Describe the morphology of the red blood cells.
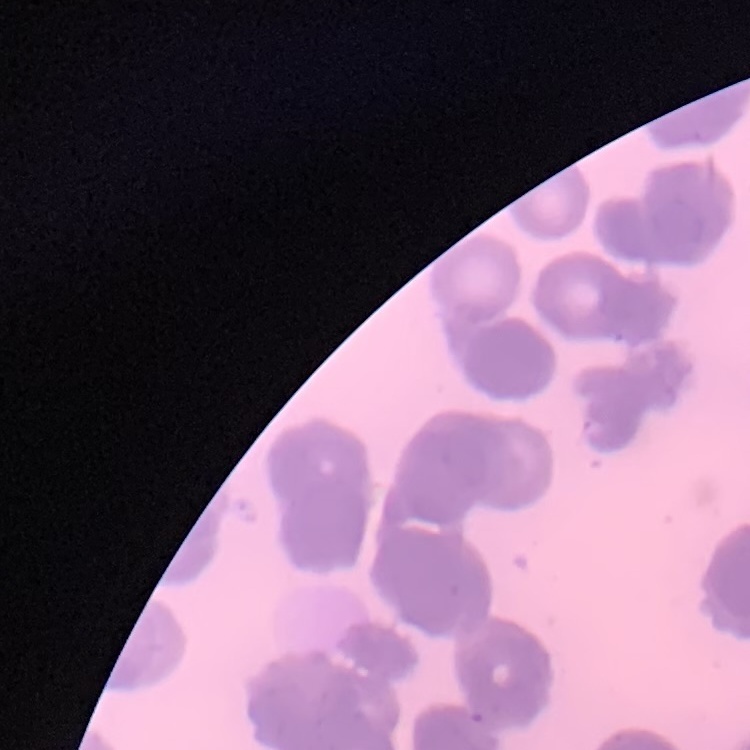

Rouleaux formation.

Summary:
  - Image type: square crop of a larger photomicrograph
  - Preparation: thin blood film
  - Stain: Field's or Giemsa